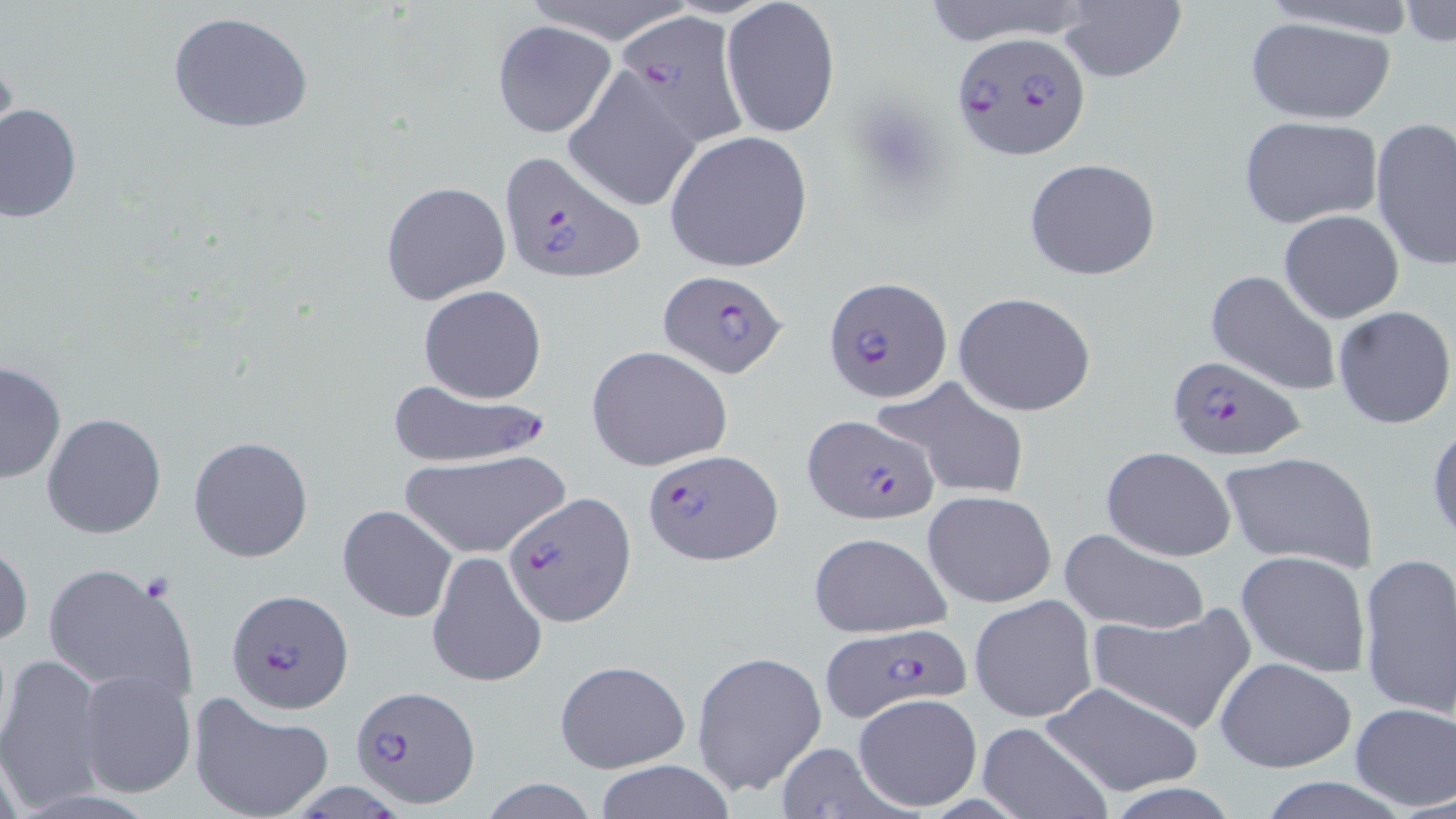

Approximate bounding boxes as (x1,y1)-(x2,y2) corner pairs in pixels. Uninfected red blood cell locations: (517,0)-(694,43), (917,0)-(1099,47), (1249,0)-(1425,38), (719,1)-(841,141), (1398,1)-(1456,48), (1054,3)-(1187,84), (166,10)-(317,135), (1245,14)-(1396,125), (491,21)-(617,139), (564,68)-(703,214), (0,103)-(82,224), (1237,114)-(1383,229), (1371,118)-(1456,270), (664,130)-(814,272), (1024,158)-(1161,281), (379,180)-(510,305), (1278,209)-(1405,324), (1205,269)-(1343,397), (418,283)-(548,403), (952,292)-(1098,416), (1332,306)-(1455,429), (585,345)-(733,472), (0,360)-(67,485), (875,376)-(1030,499), (42,412)-(166,539), (1427,419)-(1456,548), (189,435)-(314,561), (1102,446)-(1236,562), (1219,450)-(1379,574), (399,451)-(571,559), (922,489)-(1058,608), (337,503)-(459,623), (1059,527)-(1211,636), (806,531)-(953,639), (0,539)-(32,652), (1235,550)-(1371,678), (1356,550)-(1456,718), (424,552)-(547,687), (41,562)-(195,700), (968,594)-(1097,723), (1086,601)-(1257,736), (0,650)-(106,814), (691,650)-(827,798), (1214,656)-(1356,773), (554,659)-(690,774), (76,668)-(196,799), (1038,679)-(1204,799), (186,692)-(333,819), (851,693)-(983,812), (1350,702)-(1456,811), (978,719)-(1114,818), (772,743)-(909,816), (589,761)-(739,818), (1255,777)-(1413,818), (478,779)-(602,819). Plasmodium falciparum-infected red blood cell locations: (612,11)-(751,148), (951,29)-(1092,161), (496,150)-(645,285), (657,269)-(787,379), (822,274)-(953,400), (1167,354)-(1305,460), (384,378)-(553,471), (801,414)-(937,525), (642,448)-(782,567), (506,494)-(634,626), (225,587)-(353,715), (819,622)-(973,722), (351,685)-(481,808). Slide-level diagnosis: Plasmodium falciparum. May-Grünwald-Giemsa-stained preparation. Thin blood smear. 1000x magnification. One field of a larger specimen. Optical microscopy. Image is 1456×819 pixels.